Assess this cell for malaria.
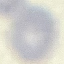
Uninfected.

image type = automatically extracted cell patch, resized to 64 × 64 pixels
stain = Giemsa
capture = smartphone through the microscope eyepiece
preparation = thin blood film